Classify this cell by malaria status.
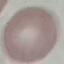

Uninfected.

stain = Giemsa
image type = cell patch, automatically extracted from a larger field of view and resized to 64 × 64 pixels
capture = smartphone through the microscope eyepiece
preparation = thin blood smear